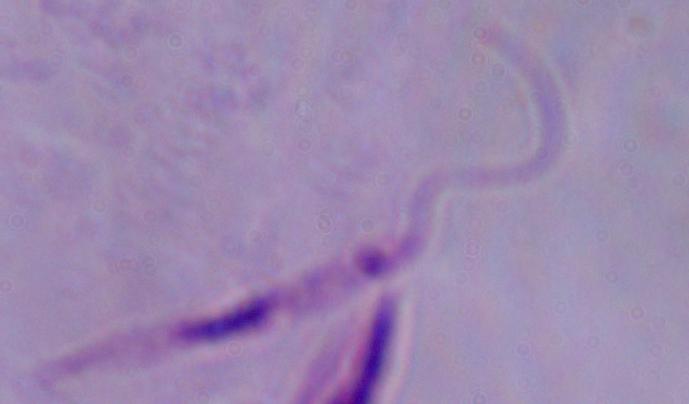

Summary:
  - Magnification: 1000x
  - Modality: micrograph
  - Identification: Leishmania